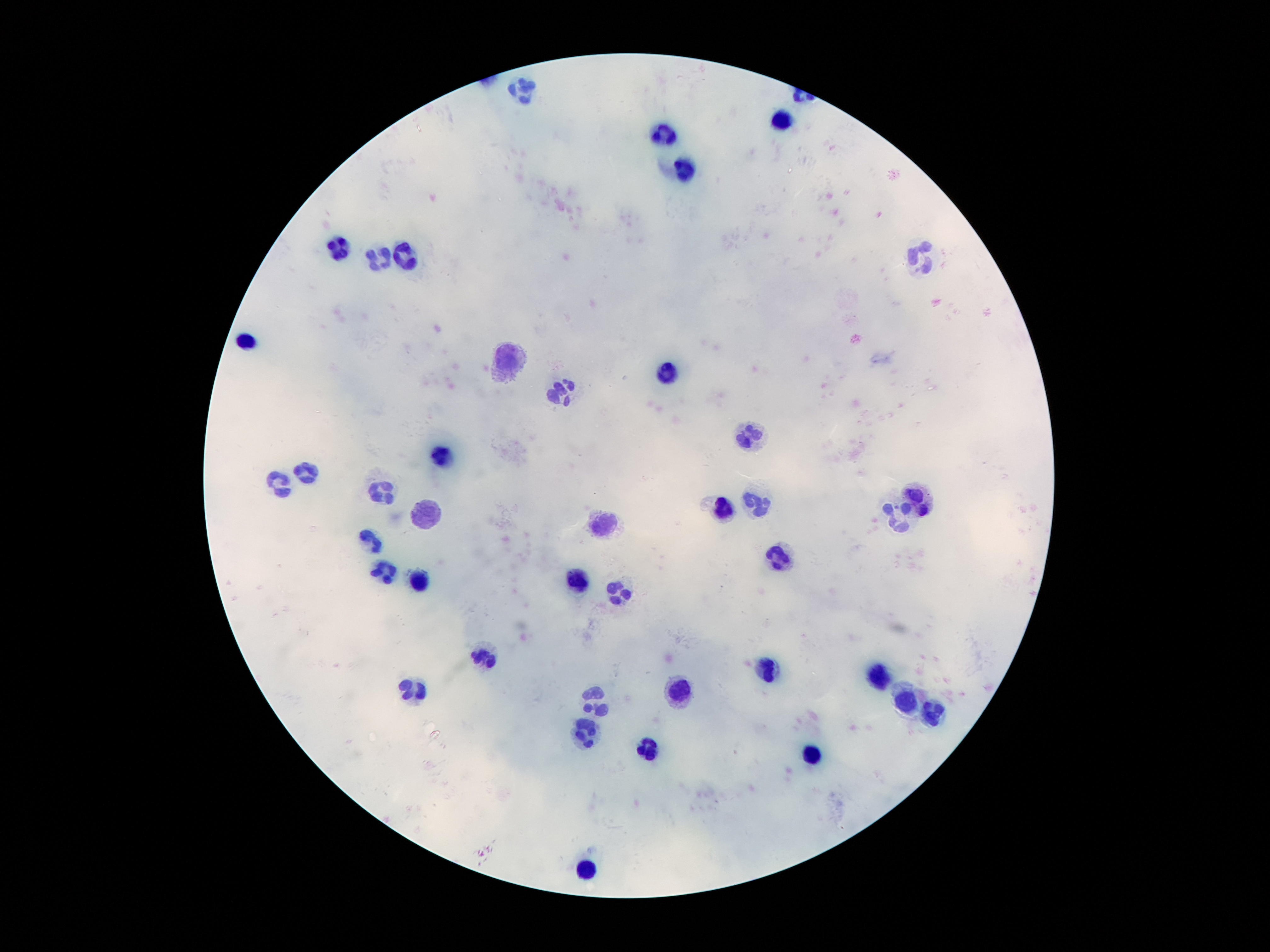

Approximate centers as (x, y) in pixels.
Summary:
  - Leukocyte locations: (523, 88), (781, 122), (663, 136), (687, 170), (339, 251), (405, 255), (921, 256), (379, 258), (247, 339), (505, 358), (665, 372), (559, 390), (747, 434), (439, 454), (307, 475), (277, 483), (379, 489), (913, 500), (721, 507), (757, 507), (421, 517), (891, 522), (603, 525), (365, 542), (775, 558), (385, 571), (419, 579), (577, 580), (615, 595), (483, 655), (763, 669), (875, 677), (677, 689), (411, 691), (591, 700), (905, 702), (933, 714), (585, 731), (649, 747), (809, 759), (581, 869)
  - Preparation: thick blood film
  - Magnification: 100x
  - Stain: Giemsa
  - Capture: smartphone camera through the microscope eyepiece
  - Field of view: single
  - Image size: 1270×952 pixels
  - Patient malaria status: negative